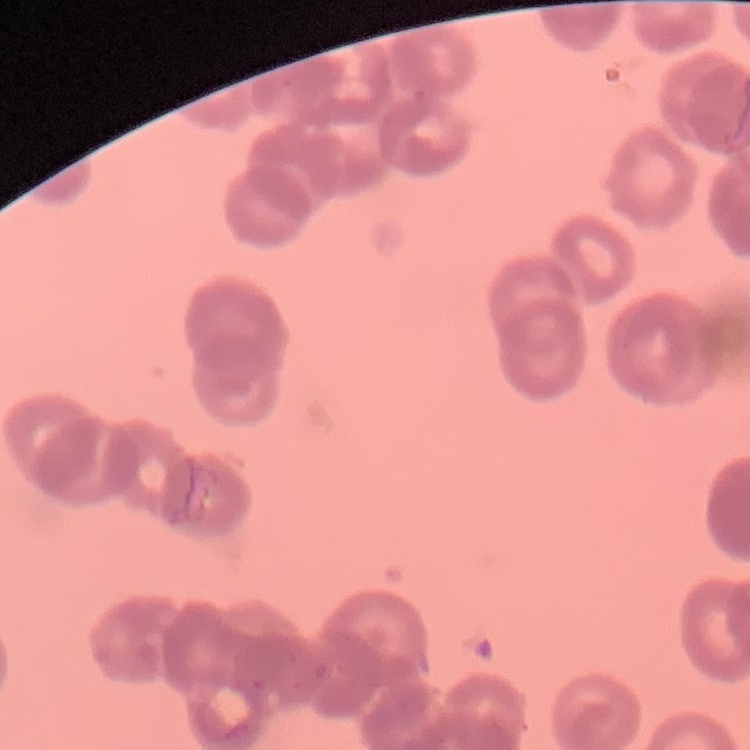
Summary:
  - Erythrocyte morphology: rouleaux formation
  - Preparation: thin blood film
  - Image type: square crop of a larger photomicrograph
  - Stain: Field's or Giemsa